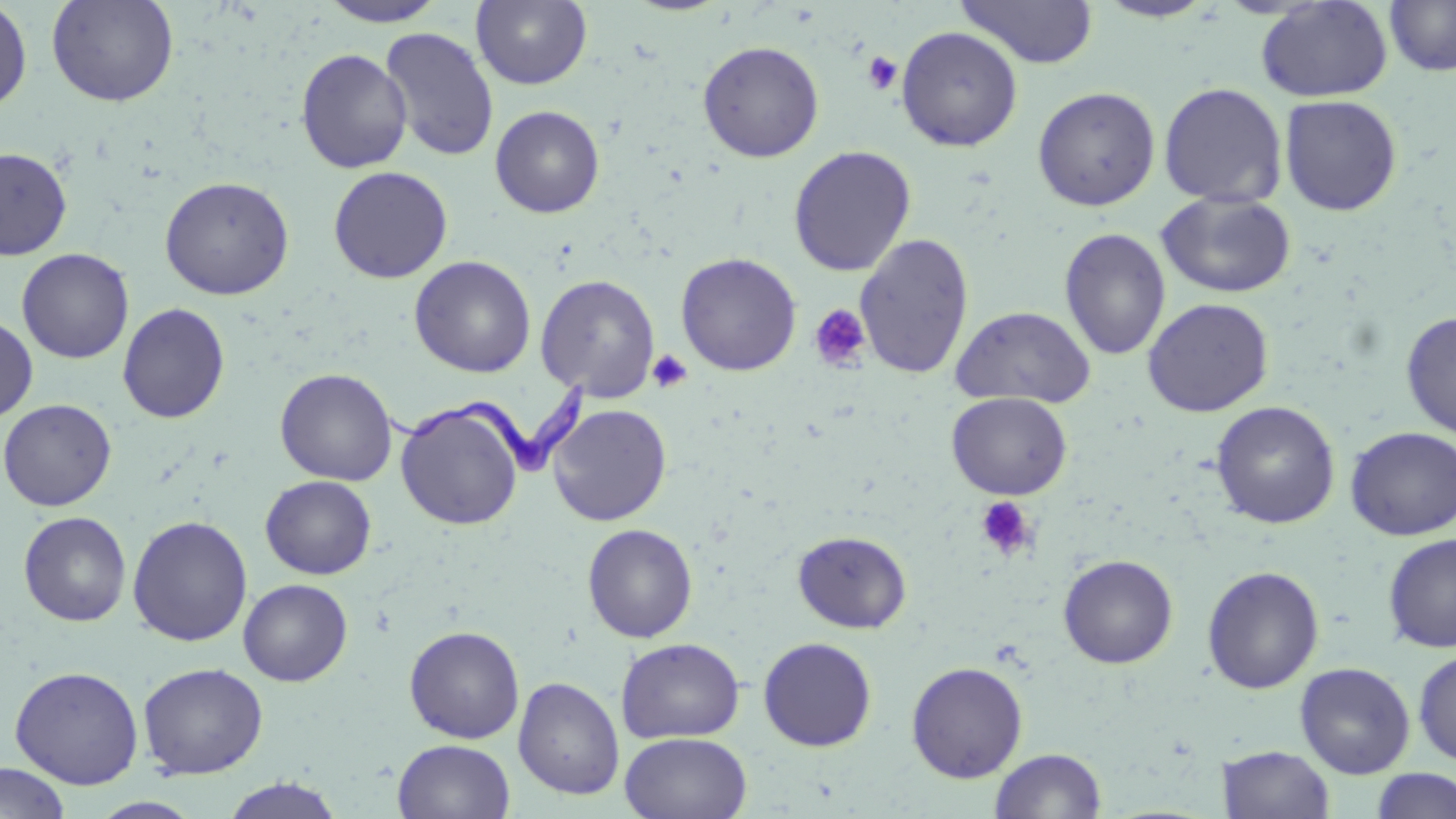

Approximate bounding boxes as named x1/y1/x2/y2 corners in pixels. Trypanosoma brucei locations: (x1=378, y1=374, x2=591, y2=476). Platelet locations: (x1=863, y1=51, x2=903, y2=95), (x1=808, y1=303, x2=872, y2=373), (x1=647, y1=349, x2=693, y2=393), (x1=975, y1=496, x2=1037, y2=561). Uninfected red blood cell locations: (x1=46, y1=0, x2=179, y2=107), (x1=316, y1=0, x2=448, y2=27), (x1=472, y1=0, x2=593, y2=89), (x1=955, y1=0, x2=1098, y2=69), (x1=1384, y1=0, x2=1456, y2=77), (x1=0, y1=1, x2=33, y2=114), (x1=1093, y1=1, x2=1219, y2=23), (x1=1255, y1=1, x2=1393, y2=103), (x1=896, y1=25, x2=1023, y2=151), (x1=380, y1=27, x2=499, y2=162), (x1=697, y1=41, x2=824, y2=162), (x1=295, y1=48, x2=413, y2=174), (x1=1158, y1=82, x2=1288, y2=207), (x1=1032, y1=86, x2=1161, y2=211), (x1=1279, y1=94, x2=1403, y2=216), (x1=490, y1=105, x2=605, y2=218), (x1=788, y1=145, x2=916, y2=277), (x1=0, y1=147, x2=72, y2=259), (x1=328, y1=165, x2=453, y2=284), (x1=159, y1=175, x2=295, y2=300), (x1=1156, y1=191, x2=1296, y2=298), (x1=1059, y1=227, x2=1171, y2=361), (x1=854, y1=232, x2=975, y2=379), (x1=17, y1=248, x2=134, y2=364), (x1=676, y1=252, x2=802, y2=376), (x1=409, y1=255, x2=536, y2=378), (x1=535, y1=274, x2=660, y2=402), (x1=1142, y1=297, x2=1274, y2=417), (x1=117, y1=303, x2=230, y2=424), (x1=950, y1=306, x2=1096, y2=409), (x1=1400, y1=311, x2=1456, y2=439), (x1=0, y1=313, x2=38, y2=424), (x1=275, y1=368, x2=398, y2=486), (x1=946, y1=391, x2=1072, y2=500), (x1=0, y1=398, x2=117, y2=511), (x1=1211, y1=400, x2=1340, y2=528), (x1=396, y1=401, x2=524, y2=530), (x1=548, y1=403, x2=672, y2=526), (x1=1345, y1=426, x2=1456, y2=540), (x1=260, y1=475, x2=377, y2=579), (x1=18, y1=511, x2=132, y2=627), (x1=127, y1=515, x2=253, y2=646), (x1=582, y1=523, x2=698, y2=643), (x1=793, y1=529, x2=912, y2=633), (x1=1382, y1=533, x2=1456, y2=652), (x1=1059, y1=554, x2=1178, y2=668), (x1=1202, y1=565, x2=1325, y2=694), (x1=238, y1=579, x2=353, y2=686), (x1=404, y1=625, x2=525, y2=743), (x1=758, y1=636, x2=877, y2=751), (x1=616, y1=637, x2=745, y2=743), (x1=1413, y1=649, x2=1456, y2=765), (x1=906, y1=661, x2=1028, y2=783), (x1=138, y1=662, x2=268, y2=779), (x1=1294, y1=662, x2=1415, y2=778), (x1=9, y1=665, x2=144, y2=789), (x1=513, y1=676, x2=625, y2=800), (x1=620, y1=732, x2=752, y2=819), (x1=393, y1=739, x2=515, y2=819), (x1=1218, y1=745, x2=1335, y2=819), (x1=989, y1=747, x2=1107, y2=819), (x1=0, y1=762, x2=70, y2=818), (x1=1370, y1=768, x2=1456, y2=819), (x1=218, y1=777, x2=347, y2=818). Slide-level diagnosis: Trypanosoma brucei. Thin blood film. May-Grünwald-Giemsa-stained preparation. One field of a larger specimen. Image is 1456×819 pixels. 1000x magnification. Light microscopy.